Describe the morphology of the red blood cells.
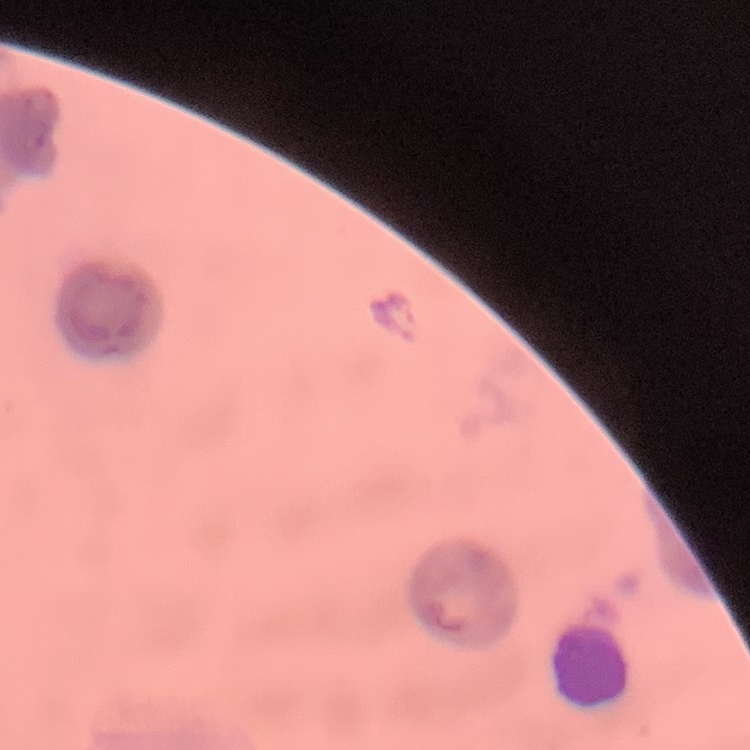

They show rouleaux formation.

image type = square crop of a larger photomicrograph
preparation = thin blood film
stain = Field's or Giemsa